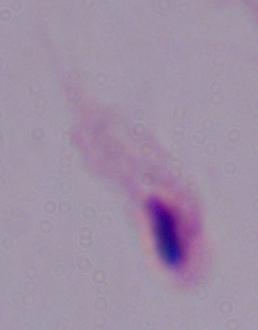

modality = photomicrograph
magnification = 1000x
identification = trichomonad